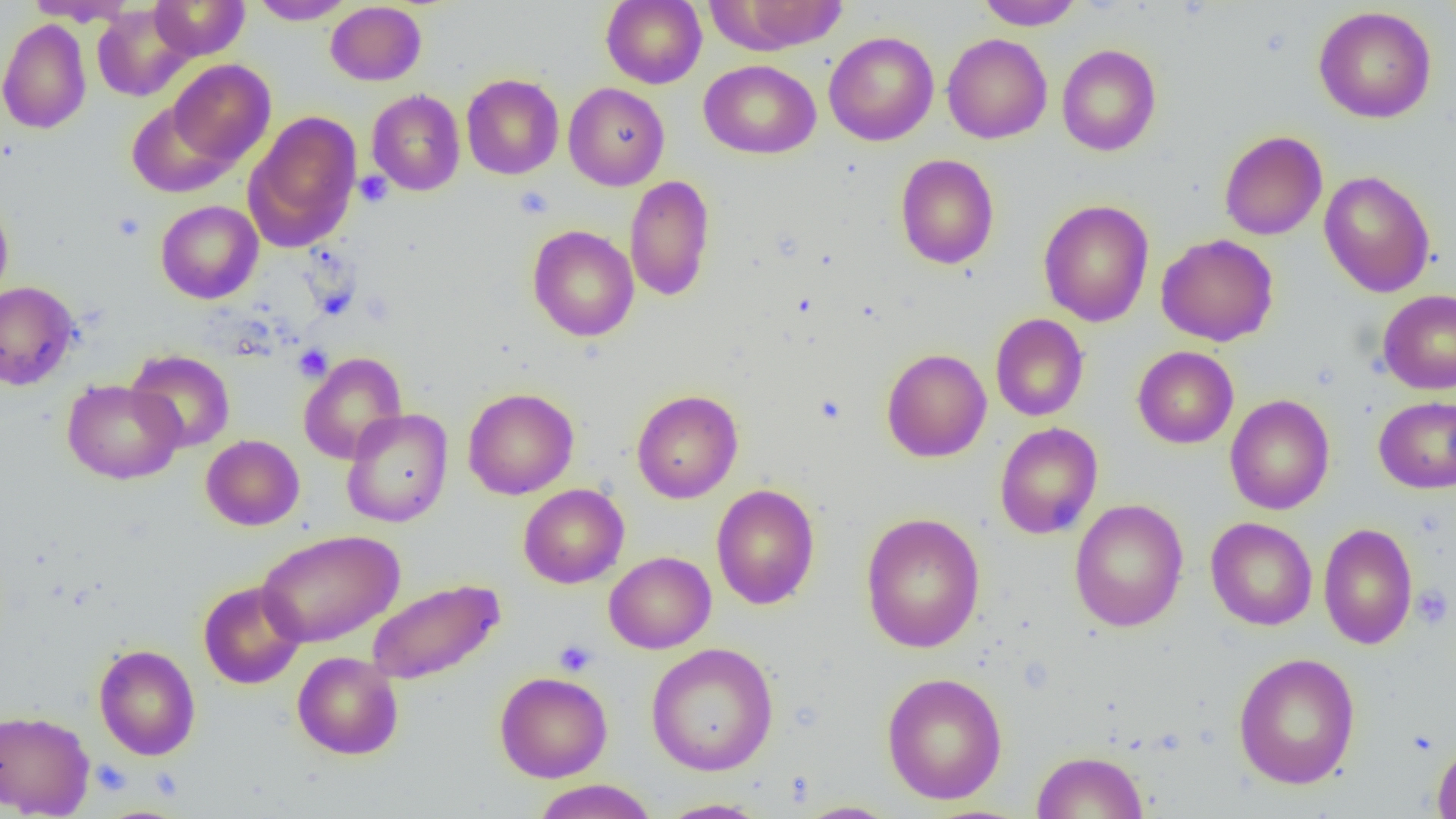

slide-level diagnosis = negative for blood parasites
magnification = 1000x
uninfected red blood cell locations = approximate bounding boxes as (x1,y1)-(x2,y2) corner pairs in pixels: (24,0)-(133,26), (149,0)-(249,60), (249,0)-(355,24), (601,0)-(707,89), (976,0)-(1084,30), (711,1)-(849,54), (325,2)-(427,86), (93,3)-(194,102), (1313,6)-(1436,123), (0,17)-(92,134), (824,31)-(939,146), (942,34)-(1052,144), (1057,44)-(1161,156), (168,59)-(276,166), (699,59)-(821,159), (461,73)-(564,179), (564,83)-(669,191), (367,89)-(466,196), (127,101)-(236,198), (244,110)-(362,251), (1219,130)-(1327,240), (895,154)-(999,270), (1318,170)-(1435,297), (624,175)-(715,302), (0,194)-(14,306), (1038,199)-(1155,327), (155,200)-(264,304), (527,225)-(639,342), (1156,233)-(1279,347), (0,281)-(79,390), (1377,289)-(1456,394), (990,314)-(1089,421), (1132,346)-(1239,448), (881,348)-(991,463), (126,350)-(235,453), (298,352)-(408,464), (61,379)-(184,484), (463,388)-(579,499), (632,389)-(743,503), (1225,394)-(1335,515), (1373,395)-(1456,494), (341,409)-(453,527), (994,422)-(1103,539), (201,435)-(304,530), (711,483)-(820,610), (518,484)-(629,588), (1069,499)-(1189,632), (860,512)-(986,653), (1205,517)-(1317,630), (1318,522)-(1418,649), (256,529)-(404,648), (604,551)-(716,654), (366,578)-(505,685), (198,580)-(307,689), (646,642)-(779,776), (93,644)-(200,760), (292,652)-(404,760), (1232,652)-(1361,790), (495,671)-(613,782), (881,672)-(1008,805), (0,708)-(94,818), (1432,740)-(1456,819), (1033,751)-(1147,818), (531,779)-(659,819), (656,798)-(770,818), (794,800)-(902,818)
platelet locations = approximate bounding boxes as (x1,y1)-(x2,y2) corner pairs in pixels: (354,171)-(393,207), (515,186)-(554,220), (112,211)-(146,241), (293,344)-(332,381), (1411,585)-(1454,629), (554,639)-(598,676), (91,759)-(131,796)
preparation = thin blood smear
image size = 1456×819 pixels
field of view = one of a larger specimen
modality = optical microscopy